Point out each leukocyte.
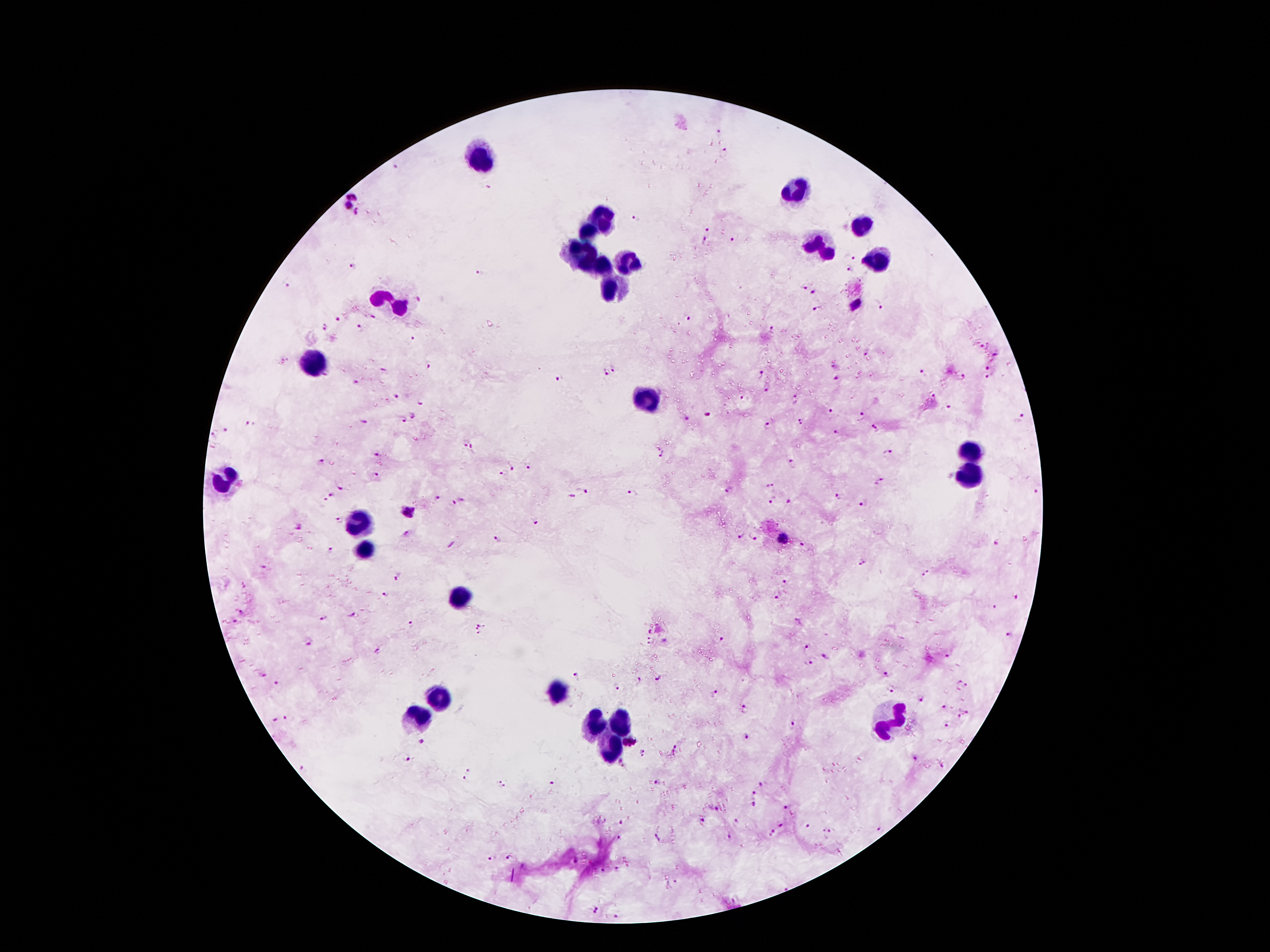

Approximate centers as (x, y) in pixels.
Leukocytes: (480, 161), (796, 192), (599, 219), (863, 226), (586, 233), (821, 247), (584, 256), (877, 259), (630, 262), (602, 267), (608, 292), (390, 302), (311, 363), (645, 399), (971, 450), (968, 475), (223, 483), (356, 521), (367, 550), (457, 596), (554, 692), (443, 700), (418, 717), (890, 720), (593, 722), (618, 723), (611, 747).

Malaria parasite locations: (718, 132), (725, 152), (397, 167), (488, 188), (354, 194), (347, 206), (359, 213), (636, 217), (708, 230), (733, 240), (703, 241), (854, 259), (351, 266), (849, 269), (481, 271), (286, 284), (803, 287), (813, 292), (418, 300), (857, 305), (878, 306), (817, 310), (687, 317), (373, 318), (338, 319), (323, 325), (360, 329), (771, 329), (413, 339), (984, 343), (866, 353), (994, 354), (283, 361), (430, 366), (833, 367), (614, 368), (985, 369), (383, 371), (919, 372), (604, 373), (761, 375), (963, 375), (835, 377), (987, 377), (560, 379), (355, 382), (767, 390), (933, 395), (397, 397), (744, 398), (794, 400), (421, 402), (949, 406), (830, 409), (708, 414), (863, 414), (1021, 415), (414, 416), (686, 418), (403, 419), (363, 421), (802, 421), (249, 425), (768, 427), (874, 427), (226, 431), (837, 433), (464, 442), (473, 449), (662, 453), (889, 453), (375, 454), (321, 462), (793, 464), (530, 466), (512, 467), (503, 473), (375, 476), (879, 482), (341, 486), (770, 486), (584, 488), (730, 489), (1035, 490), (632, 493), (331, 494), (840, 496), (436, 497), (572, 497), (462, 498), (772, 500), (325, 501), (788, 502), (453, 503), (864, 503), (407, 512), (339, 520), (535, 521), (299, 527), (407, 532), (740, 534), (755, 535), (782, 538), (497, 540), (994, 543), (804, 546), (330, 551), (863, 562), (263, 568), (928, 574), (398, 577), (785, 582), (385, 594), (1017, 597), (776, 599), (995, 607), (241, 611), (352, 614), (324, 618), (236, 623), (411, 624), (479, 628), (649, 632), (1009, 635), (721, 640), (308, 642), (650, 642), (806, 647), (377, 653), (825, 656), (948, 656), (812, 662), (887, 674), (262, 675), (575, 675), (659, 677), (636, 679), (959, 682), (277, 685), (968, 685), (615, 687), (889, 688), (958, 689), (715, 694), (920, 700), (943, 708), (745, 709), (965, 710), (960, 717), (288, 718), (276, 721), (793, 725), (947, 725), (747, 738), (425, 741), (631, 741), (674, 749), (643, 753), (408, 758), (913, 758), (622, 764), (942, 766), (468, 771), (303, 772), (463, 780), (657, 781), (761, 784), (499, 785), (553, 785), (751, 791), (754, 803), (716, 807), (786, 808), (738, 820), (702, 821), (620, 822), (781, 825), (807, 826), (881, 828), (826, 829), (772, 831), (730, 836), (657, 839), (619, 840), (509, 856), (492, 858), (618, 870), (603, 872), (675, 883), (595, 910), (615, 917). Patient malaria status: positive for Plasmodium falciparum. Giemsa-stained preparation. Smartphone photograph taken through the microscope eyepiece. Image is 1270×952 pixels. 100x magnification. One field from this slide. Thick blood film.